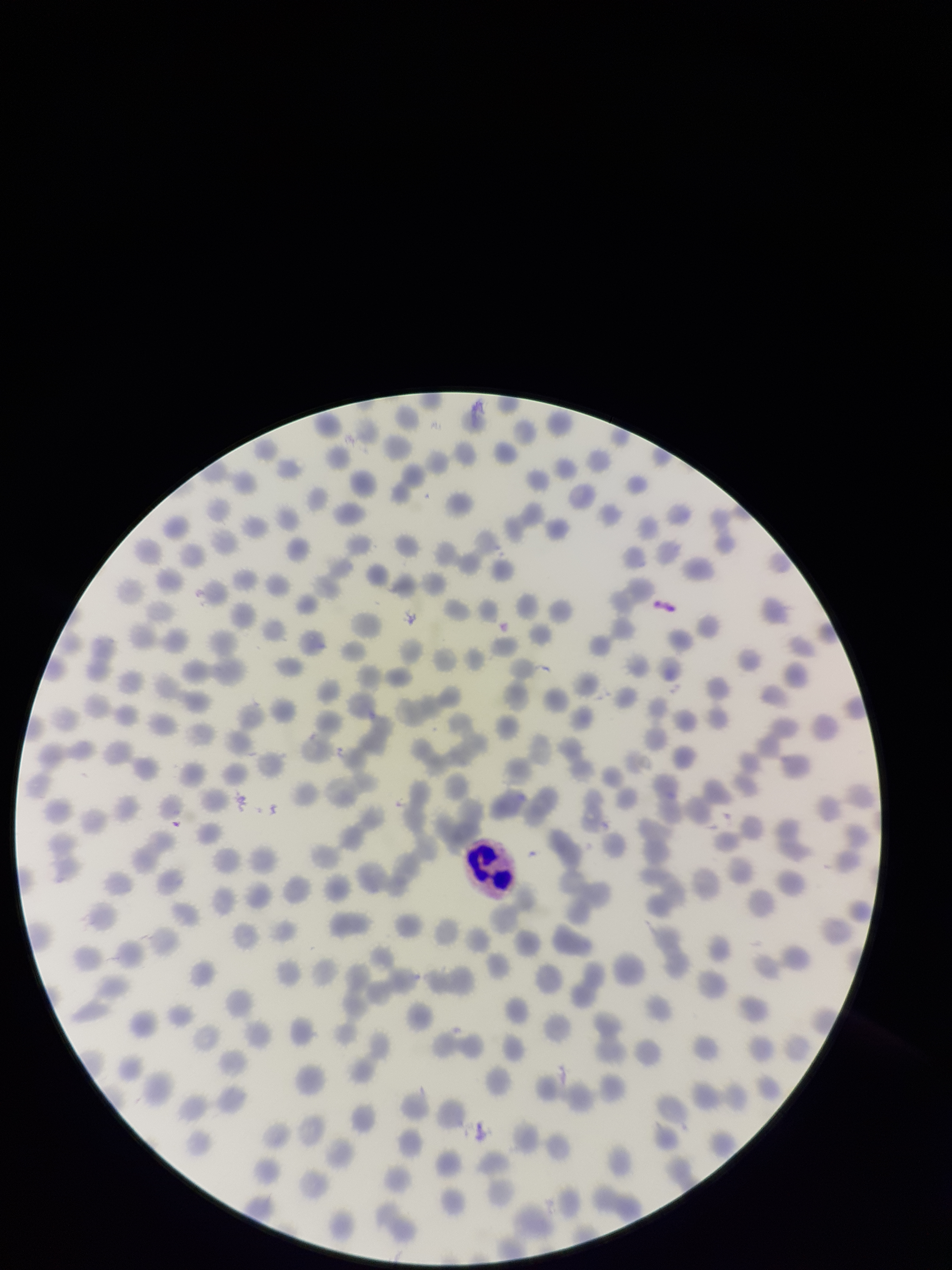
Parasitized red blood cell count: 0. Single field of view. Photographed through the microscope eyepiece with a smartphone camera. Patient malaria status: infected. Giemsa stain. Species reported for this patient: Plasmodium falciparum. Preparation: thin smear. Red blood cell count: 287. Image is 952×1270 pixels. Parasitized red blood cells: none seen.